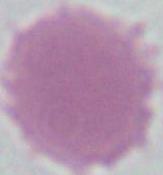

Captured at 1000x magnification. Micrograph. An erythrocyte is seen.